Describe the morphology of the red blood cells.
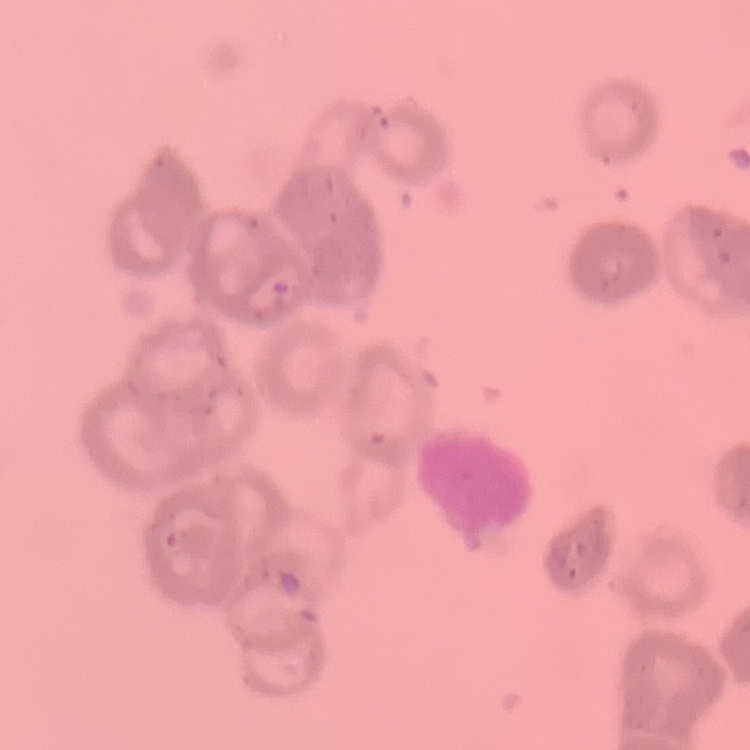

Rouleaux formation.

stain = Field's or Giemsa
preparation = thin blood film
image type = square crop of a larger photomicrograph